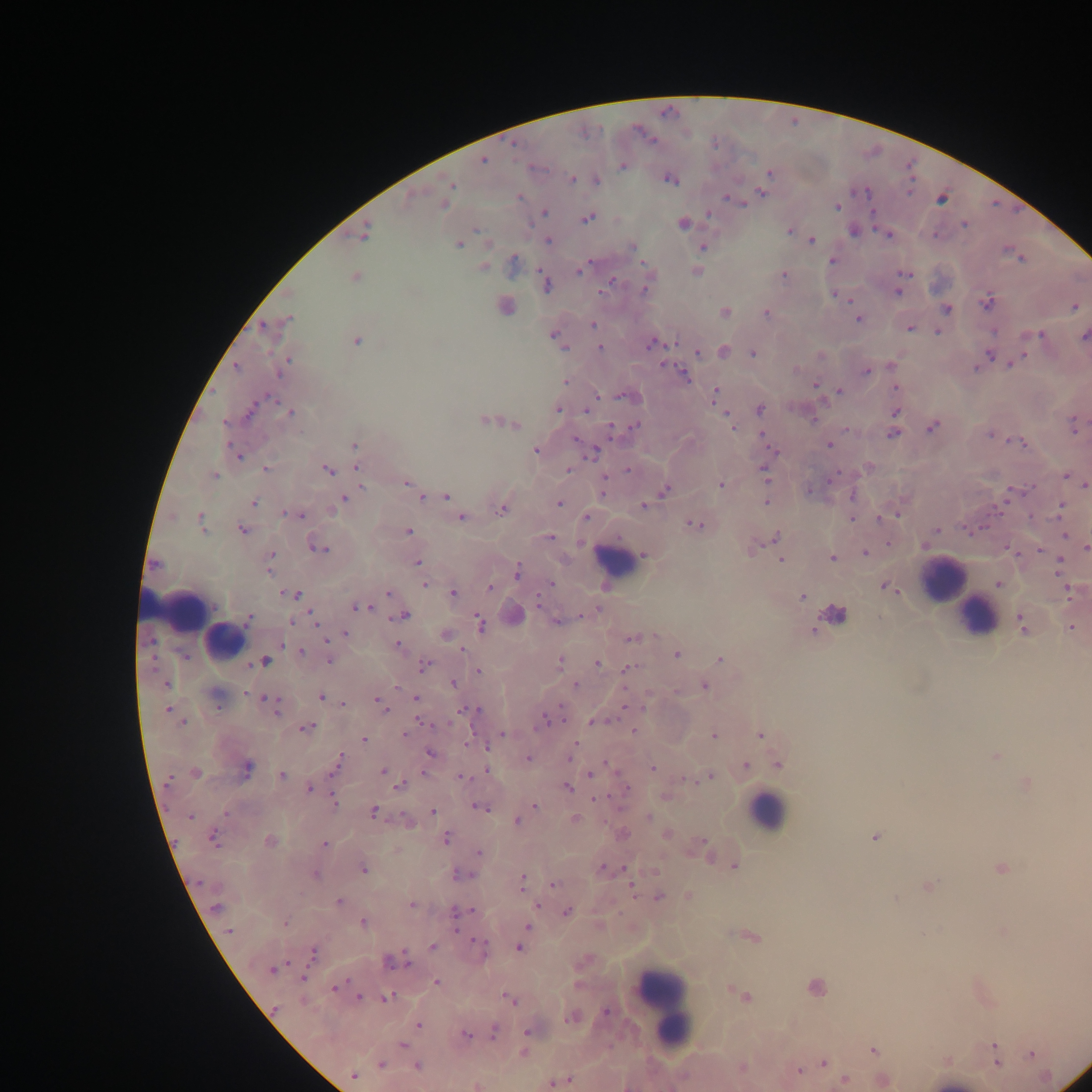

Approximate centers as {x, y} in pixels.
Summary:
  - Malaria parasite locations: {515, 145}, {483, 161}, {623, 165}, {769, 172}, {572, 179}, {670, 179}, {597, 181}, {450, 185}, {761, 193}, {518, 197}, {942, 199}, {734, 200}, {444, 205}, {837, 207}, {544, 212}, {709, 214}, {588, 218}, {683, 224}, {965, 225}, {789, 231}, {853, 231}, {364, 232}, {888, 235}, {547, 240}, {812, 240}, {459, 245}, {632, 246}, {703, 247}, {1021, 258}, {832, 261}, {513, 262}, {483, 267}, {579, 271}, {696, 271}, {904, 273}, {783, 274}, {356, 277}, {613, 281}, {546, 284}, {645, 291}, {897, 292}, {840, 295}, {988, 302}, {505, 306}, {1074, 307}, {947, 309}, {725, 312}, {766, 313}, {289, 319}, {859, 320}, {593, 325}, {264, 326}, {910, 328}, {938, 331}, {993, 331}, {1037, 335}, {1084, 336}, {555, 338}, {357, 342}, {651, 343}, {600, 348}, {724, 351}, {698, 353}, {752, 354}, {989, 354}, {1015, 362}, {892, 366}, {237, 367}, {283, 367}, {797, 368}, {976, 368}, {865, 371}, {684, 374}, {566, 382}, {816, 387}, {896, 388}, {838, 391}, {715, 394}, {625, 397}, {558, 409}, {759, 409}, {588, 410}, {249, 412}, {290, 412}, {896, 412}, {813, 420}, {485, 421}, {225, 423}, {731, 423}, {515, 425}, {1073, 426}, {634, 427}, {932, 428}, {612, 431}, {761, 434}, {894, 434}, {990, 436}, {1020, 443}, {829, 445}, {355, 446}, {535, 451}, {591, 452}, {238, 455}, {869, 467}, {358, 468}, {266, 469}, {327, 470}, {567, 470}, {628, 470}, {764, 473}, {214, 476}, {834, 476}, {1068, 477}, {407, 484}, {361, 485}, {721, 485}, {1085, 485}, {665, 489}, {422, 497}, {446, 497}, {852, 497}, {344, 499}, {766, 502}, {254, 503}, {559, 504}, {643, 506}, {1061, 506}, {501, 511}, {286, 513}, {299, 515}, {586, 517}, {200, 518}, {462, 518}, {881, 518}, {851, 520}, {201, 525}, {695, 525}, {969, 528}, {243, 530}, {936, 530}, {408, 532}, {1065, 536}, {549, 537}, {776, 537}, {1086, 547}, {753, 548}, {319, 549}, {1040, 551}, {865, 553}, {271, 554}, {644, 555}, {833, 559}, {781, 560}, {417, 562}, {155, 564}, {1059, 564}, {269, 572}, {518, 572}, {550, 583}, {425, 585}, {999, 585}, {490, 587}, {886, 587}, {1069, 591}, {388, 593}, {453, 593}, {294, 594}, {802, 596}, {538, 603}, {357, 607}, {366, 607}, {596, 610}, {403, 615}, {314, 617}, {249, 618}, {293, 621}, {558, 621}, {480, 623}, {1022, 624}, {1071, 628}, {813, 631}, {346, 633}, {445, 635}, {631, 638}, {398, 645}, {462, 649}, {301, 651}, {677, 654}, {184, 656}, {329, 660}, {719, 660}, {265, 661}, {560, 663}, {597, 663}, {424, 666}, {627, 667}, {478, 671}, {454, 683}, {166, 684}, {575, 685}, {705, 686}, {320, 697}, {266, 698}, {416, 698}, {377, 700}, {342, 703}, {381, 706}, {168, 709}, {463, 709}, {472, 709}, {277, 710}, {546, 720}, {595, 721}, {182, 723}, {307, 727}, {633, 731}, {404, 734}, {503, 734}, {760, 735}, {713, 736}, {364, 740}, {430, 754}, {570, 756}, {996, 756}, {528, 758}, {339, 762}, {745, 764}, {779, 765}, {653, 768}, {246, 769}, {195, 772}, {383, 772}, {485, 772}, {592, 774}, {282, 775}, {711, 776}, {461, 777}, {169, 780}, {687, 780}, {400, 786}, {568, 787}, {627, 788}, {310, 789}, {595, 799}, {335, 802}, {535, 806}, {479, 807}, {225, 812}, {374, 812}, {432, 812}, {190, 816}, {649, 817}, {575, 819}, {517, 820}, {667, 835}, {875, 837}, {213, 838}, {447, 838}, {270, 841}, {703, 844}, {325, 845}, {479, 853}, {735, 866}, {1001, 868}, {363, 869}, {603, 869}, {315, 875}, {462, 875}, {522, 882}, {554, 884}, {928, 886}, {632, 890}, {659, 897}, {896, 899}, {340, 901}, {411, 904}, {535, 905}, {216, 908}, {458, 912}, {567, 912}, {362, 922}, {285, 923}, {528, 927}, {456, 928}, {230, 931}, {752, 937}, {481, 942}, {432, 946}, {519, 948}, {314, 952}, {392, 962}, {273, 970}, {303, 978}, {436, 983}, {816, 987}, {334, 988}, {737, 992}, {745, 997}, {359, 998}, {387, 998}, {509, 999}, {274, 1008}, {607, 1012}, {571, 1018}, {418, 1025}, {527, 1031}, {494, 1032}, {465, 1034}, {403, 1044}, {994, 1045}, {873, 1050}, {523, 1053}, {995, 1054}, {1031, 1055}, {997, 1062}, {824, 1063}, {381, 1065}, {417, 1066}, {798, 1071}, {354, 1076}, {845, 1079}, {566, 1081}, {558, 1082}
  - Leukocyte locations: {610, 556}, {942, 580}, {190, 612}, {977, 617}, {767, 811}, {664, 1004}
  - Preparation: thick blood film
  - Image size: 1092×1092 pixels
  - Country: Ghana
  - Capture: mobile-phone photograph through a microscope
  - Field of view: single